Describe the morphology of the erythrocytes.
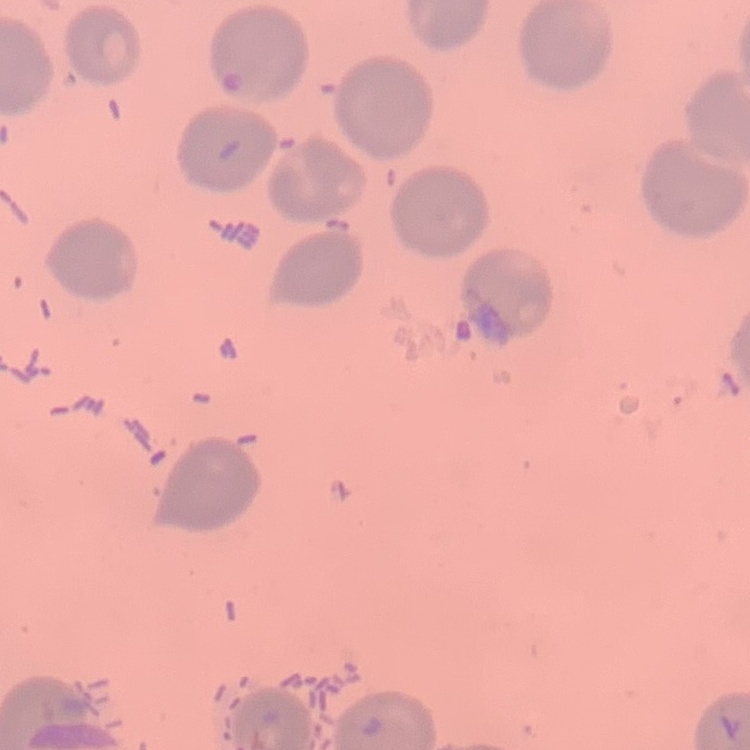

No rouleaux formation.

Field's or Giemsa stain. Thin blood film. Square crop of a larger photomicrograph.